State the blood parasite species.
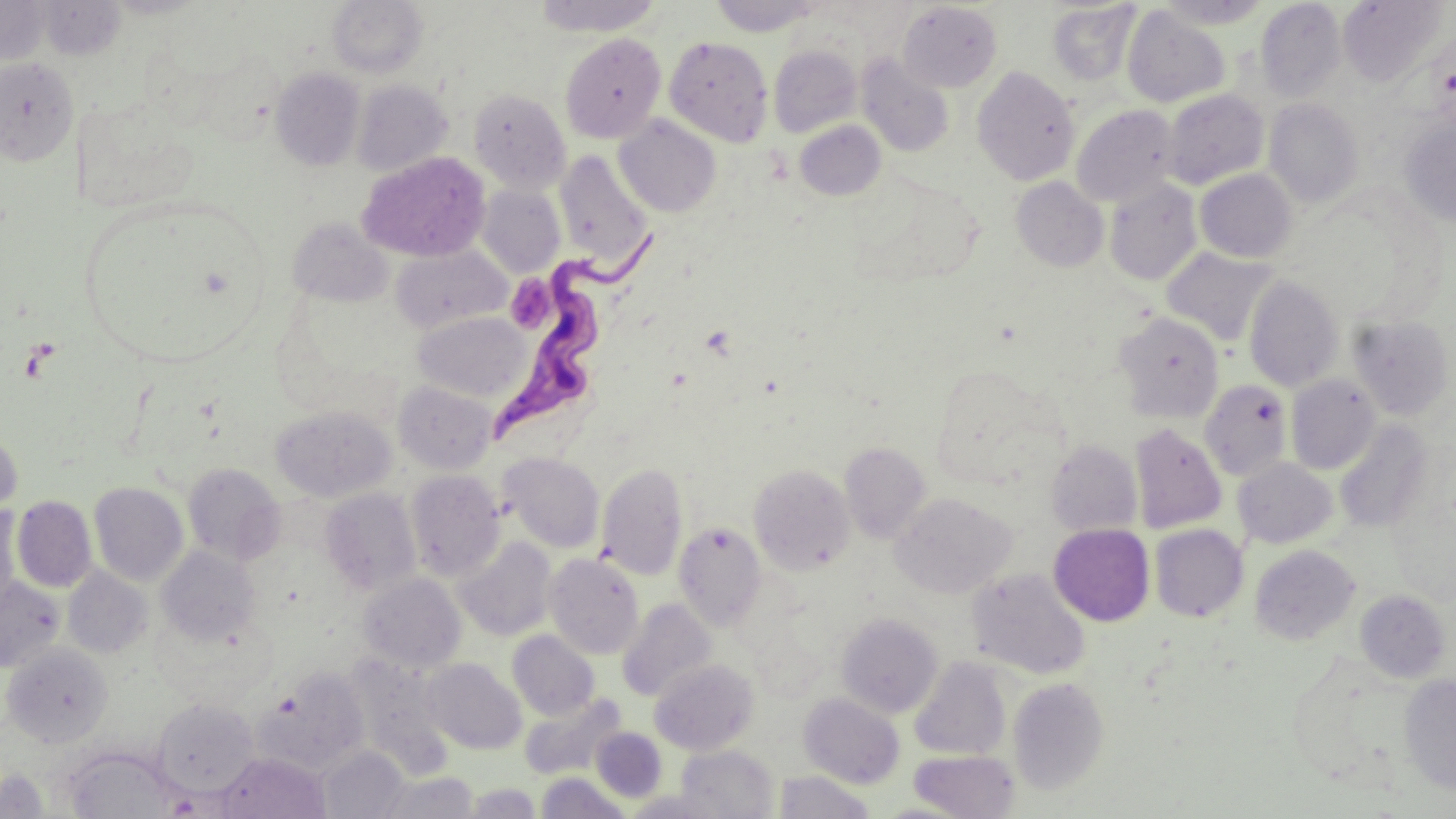

Trypanosoma brucei.

{
  "field_of_view": "one of a larger specimen",
  "platelet_locations": "approximate bounding boxes as named x1/y1/x2/y2 corners in pixels: (x1=505, y1=276, x2=554, y2=334)",
  "stain": "May-Grünwald-Giemsa",
  "preparation": "thin blood film",
  "image_size": "1456×819 pixels",
  "uninfected_red_blood_cell_locations": "approximate bounding boxes as named x1/y1/x2/y2 corners in pixels: (x1=0, y1=0, x2=51, y2=68), (x1=327, y1=0, x2=429, y2=79), (x1=533, y1=0, x2=665, y2=37), (x1=709, y1=0, x2=822, y2=36), (x1=1155, y1=0, x2=1272, y2=29), (x1=1341, y1=0, x2=1445, y2=88), (x1=39, y1=1, x2=127, y2=60), (x1=1255, y1=1, x2=1346, y2=101), (x1=898, y1=2, x2=1003, y2=93), (x1=1047, y1=2, x2=1140, y2=85), (x1=1122, y1=6, x2=1229, y2=108), (x1=560, y1=34, x2=666, y2=143), (x1=664, y1=35, x2=773, y2=147), (x1=768, y1=44, x2=862, y2=137), (x1=857, y1=54, x2=954, y2=158), (x1=0, y1=56, x2=79, y2=166), (x1=271, y1=67, x2=365, y2=171), (x1=972, y1=67, x2=1080, y2=185), (x1=351, y1=80, x2=452, y2=176), (x1=469, y1=88, x2=571, y2=193), (x1=1162, y1=89, x2=1269, y2=190), (x1=1265, y1=98, x2=1364, y2=206), (x1=1071, y1=105, x2=1179, y2=207), (x1=613, y1=115, x2=722, y2=217), (x1=1400, y1=118, x2=1456, y2=227), (x1=794, y1=120, x2=887, y2=201), (x1=358, y1=151, x2=490, y2=261), (x1=555, y1=151, x2=654, y2=273), (x1=1195, y1=169, x2=1297, y2=263), (x1=1011, y1=177, x2=1108, y2=272), (x1=1104, y1=178, x2=1202, y2=286), (x1=477, y1=184, x2=565, y2=277), (x1=286, y1=216, x2=393, y2=307), (x1=391, y1=244, x2=510, y2=334), (x1=1162, y1=247, x2=1277, y2=346), (x1=1244, y1=275, x2=1344, y2=391), (x1=412, y1=311, x2=532, y2=403), (x1=1115, y1=311, x2=1224, y2=422), (x1=1347, y1=313, x2=1454, y2=421), (x1=1285, y1=375, x2=1381, y2=475), (x1=1199, y1=380, x2=1292, y2=481), (x1=393, y1=381, x2=498, y2=474), (x1=270, y1=406, x2=396, y2=502), (x1=1334, y1=419, x2=1435, y2=533), (x1=1129, y1=422, x2=1227, y2=534), (x1=0, y1=427, x2=22, y2=522), (x1=1045, y1=439, x2=1142, y2=537), (x1=839, y1=442, x2=931, y2=543), (x1=499, y1=452, x2=605, y2=553), (x1=1233, y1=458, x2=1337, y2=549), (x1=596, y1=462, x2=688, y2=580), (x1=182, y1=463, x2=285, y2=565), (x1=749, y1=464, x2=854, y2=576), (x1=404, y1=470, x2=505, y2=580), (x1=89, y1=482, x2=188, y2=585), (x1=319, y1=488, x2=423, y2=596), (x1=890, y1=492, x2=1017, y2=599), (x1=12, y1=496, x2=97, y2=592), (x1=0, y1=504, x2=21, y2=614), (x1=674, y1=522, x2=767, y2=630), (x1=1048, y1=523, x2=1155, y2=626), (x1=1149, y1=524, x2=1248, y2=622), (x1=455, y1=537, x2=556, y2=641), (x1=1249, y1=544, x2=1360, y2=646), (x1=157, y1=546, x2=261, y2=646), (x1=544, y1=553, x2=644, y2=659), (x1=63, y1=567, x2=153, y2=658), (x1=966, y1=567, x2=1092, y2=679), (x1=358, y1=572, x2=467, y2=674), (x1=0, y1=576, x2=66, y2=673), (x1=1354, y1=589, x2=1451, y2=683), (x1=617, y1=598, x2=717, y2=703), (x1=836, y1=612, x2=943, y2=718), (x1=507, y1=630, x2=600, y2=721), (x1=2, y1=643, x2=113, y2=747), (x1=347, y1=656, x2=453, y2=773), (x1=909, y1=657, x2=1011, y2=761), (x1=422, y1=658, x2=526, y2=755), (x1=650, y1=659, x2=758, y2=754), (x1=257, y1=666, x2=370, y2=775), (x1=1398, y1=674, x2=1456, y2=796), (x1=1007, y1=676, x2=1110, y2=795), (x1=520, y1=691, x2=626, y2=781), (x1=799, y1=693, x2=905, y2=789), (x1=153, y1=698, x2=260, y2=796), (x1=591, y1=728, x2=667, y2=802), (x1=675, y1=745, x2=779, y2=819), (x1=319, y1=746, x2=409, y2=819), (x1=908, y1=749, x2=1020, y2=818), (x1=215, y1=752, x2=330, y2=819), (x1=67, y1=754, x2=182, y2=818), (x1=0, y1=768, x2=51, y2=817), (x1=378, y1=769, x2=480, y2=818), (x1=774, y1=770, x2=875, y2=819), (x1=535, y1=772, x2=631, y2=818), (x1=463, y1=780, x2=544, y2=818)",
  "trypanosoma_brucei_locations": "approximate bounding boxes as named x1/y1/x2/y2 corners in pixels: (x1=492, y1=229, x2=665, y2=448)",
  "magnification": "1000x",
  "modality": "optical microscopy"
}